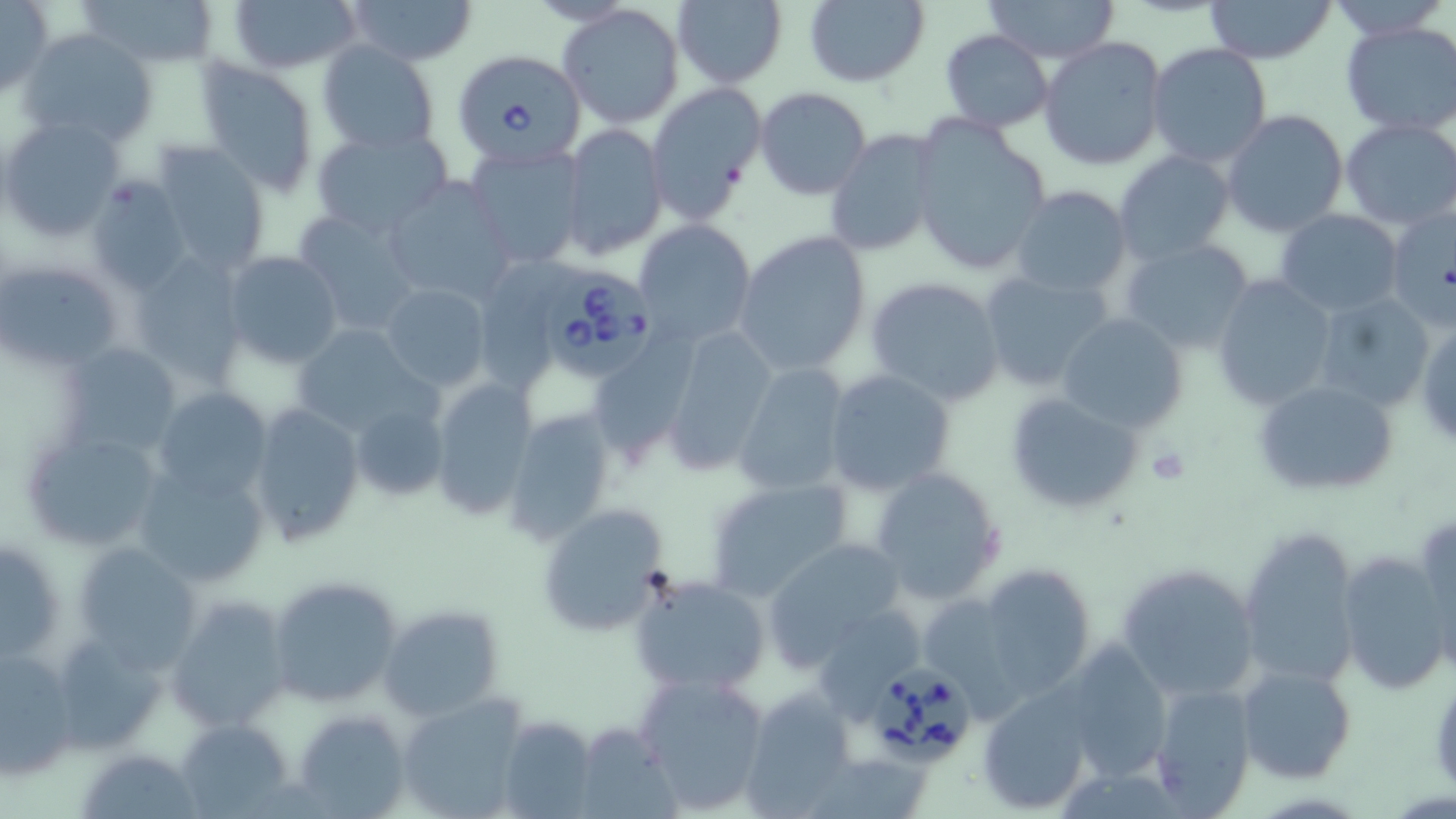

Summary:
  - Coordinate format: approximate bounding boxes as (x1, y1, x2, y2) in pixels
  - Uninfected red blood cell locations: (0, 0, 52, 96), (78, 0, 220, 68), (228, 0, 361, 74), (344, 0, 478, 65), (673, 0, 788, 88), (804, 0, 929, 86), (978, 0, 1120, 64), (1202, 0, 1334, 64), (1328, 0, 1448, 40), (560, 4, 685, 128), (1339, 21, 1456, 135), (19, 28, 157, 150), (940, 30, 1054, 132), (1040, 37, 1168, 171), (317, 41, 439, 154), (1146, 43, 1273, 168), (196, 58, 320, 196), (646, 83, 766, 221), (755, 87, 871, 200), (1222, 109, 1349, 235), (0, 116, 125, 244), (910, 116, 1051, 276), (1339, 117, 1456, 231), (558, 123, 668, 262), (310, 128, 453, 239), (825, 128, 944, 259), (151, 142, 271, 274), (465, 142, 588, 268), (1113, 149, 1236, 263), (381, 175, 514, 304), (86, 179, 190, 293), (1011, 185, 1132, 297), (1386, 203, 1455, 331), (291, 209, 422, 334), (1275, 209, 1403, 313), (631, 219, 758, 347), (734, 231, 871, 376), (1119, 238, 1256, 354), (129, 248, 249, 377), (223, 252, 343, 366), (483, 256, 581, 397), (2, 259, 121, 369), (976, 268, 1115, 392), (1209, 273, 1338, 412), (866, 275, 1004, 407), (379, 284, 491, 391), (1314, 291, 1435, 413), (1057, 312, 1187, 432), (1416, 321, 1456, 451), (289, 323, 435, 442), (661, 323, 777, 475), (594, 329, 702, 470), (58, 340, 186, 459), (731, 364, 851, 497), (824, 368, 956, 495), (429, 380, 537, 521), (1255, 380, 1399, 496), (150, 387, 274, 507), (1005, 390, 1147, 515), (344, 395, 454, 506), (247, 403, 365, 547), (502, 408, 617, 544), (22, 427, 168, 554), (134, 463, 272, 591), (867, 466, 1006, 604), (703, 476, 854, 600), (536, 505, 669, 634), (1414, 511, 1455, 660), (1236, 526, 1360, 690), (2, 533, 66, 670), (764, 538, 909, 668), (71, 542, 202, 670), (1338, 550, 1452, 694), (978, 562, 1098, 700), (1115, 563, 1261, 706), (267, 573, 406, 708), (632, 574, 770, 696), (168, 597, 295, 733), (926, 599, 1026, 726), (380, 605, 506, 723), (817, 606, 922, 727), (48, 629, 171, 755), (1061, 640, 1170, 782), (1, 648, 79, 778), (1236, 662, 1356, 784), (635, 672, 771, 813), (1147, 680, 1257, 816), (977, 683, 1098, 815), (743, 687, 855, 813), (396, 693, 531, 819), (294, 708, 411, 817), (502, 715, 595, 819), (177, 718, 296, 817), (574, 723, 681, 817), (82, 747, 202, 817)
  - Babesia divergens-infected red blood cell locations: (451, 48, 587, 169), (540, 274, 654, 382), (871, 665, 973, 761)
  - Platelet locations: (1145, 447, 1190, 487)
  - Slide-level diagnosis: Babesia divergens
  - Magnification: 1000x
  - Preparation: thin blood film
  - Field of view: one of a larger specimen
  - Modality: optical microscopy
  - Stain: May-Grünwald-Giemsa
  - Image size: 1456×819 pixels